Identify the blood parasite species.
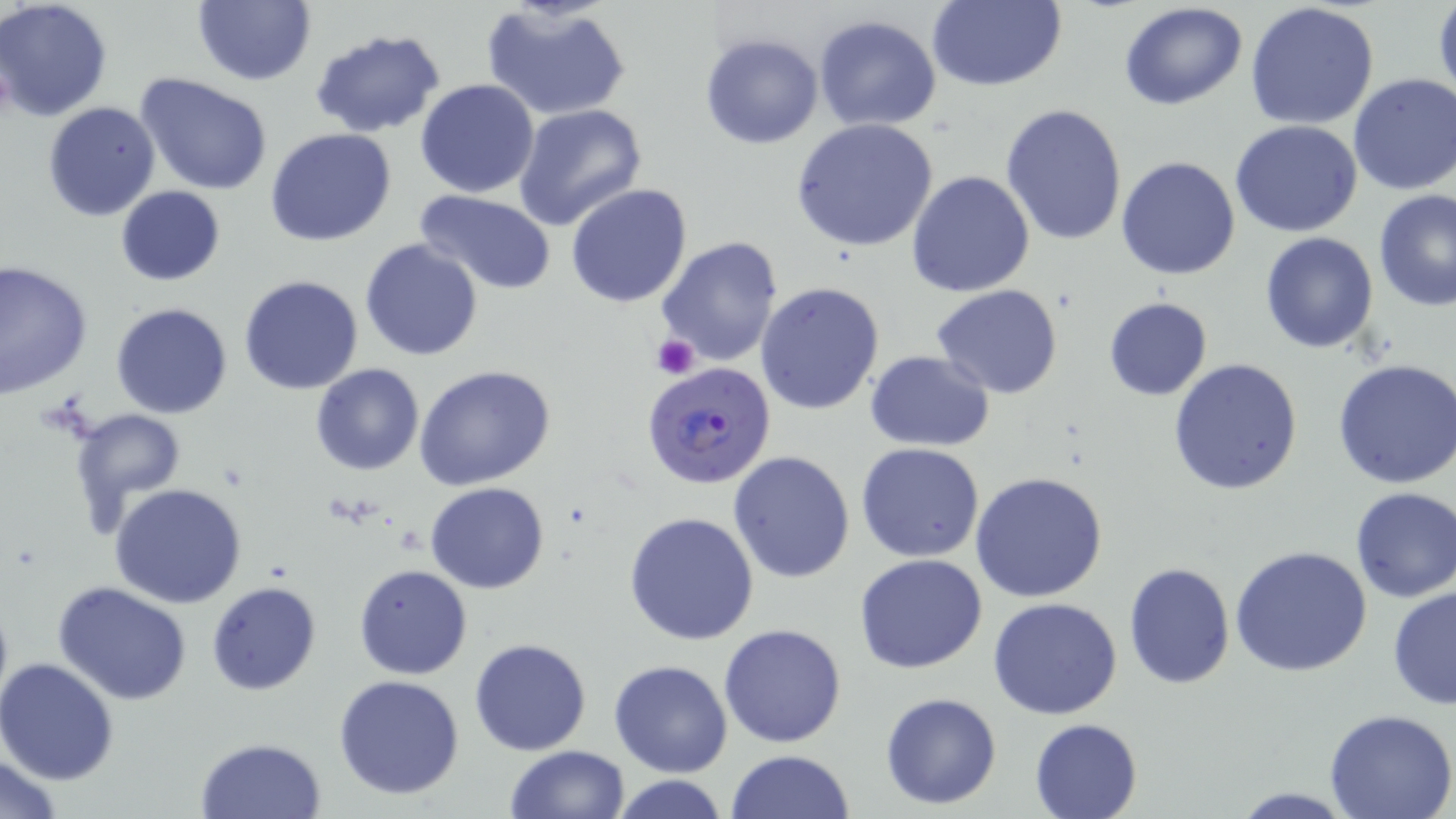

Plasmodium falciparum.

Summary:
  - Coordinate format: approximate bounding boxes as named x1/y1/x2/y2 corners in pixels
  - Platelet locations: (x1=652, y1=333, x2=700, y2=379)
  - Plasmodium falciparum-infected red blood cell locations: (x1=644, y1=361, x2=776, y2=487)
  - Uninfected red blood cell locations: (x1=0, y1=0, x2=114, y2=122), (x1=192, y1=0, x2=315, y2=86), (x1=924, y1=0, x2=1066, y2=91), (x1=480, y1=2, x2=632, y2=123), (x1=1120, y1=2, x2=1249, y2=111), (x1=1244, y1=2, x2=1380, y2=130), (x1=1432, y1=3, x2=1456, y2=104), (x1=813, y1=15, x2=943, y2=132), (x1=310, y1=29, x2=445, y2=137), (x1=699, y1=32, x2=825, y2=150), (x1=135, y1=72, x2=274, y2=196), (x1=1348, y1=72, x2=1456, y2=196), (x1=414, y1=80, x2=540, y2=199), (x1=44, y1=101, x2=160, y2=221), (x1=513, y1=104, x2=647, y2=231), (x1=1000, y1=104, x2=1128, y2=249), (x1=790, y1=117, x2=940, y2=254), (x1=1229, y1=119, x2=1362, y2=238), (x1=265, y1=128, x2=397, y2=247), (x1=1116, y1=155, x2=1240, y2=281), (x1=906, y1=169, x2=1035, y2=298), (x1=565, y1=183, x2=693, y2=307), (x1=115, y1=185, x2=225, y2=286), (x1=415, y1=191, x2=558, y2=295), (x1=1374, y1=191, x2=1456, y2=312), (x1=1260, y1=232, x2=1378, y2=353), (x1=656, y1=236, x2=785, y2=369), (x1=359, y1=239, x2=484, y2=361), (x1=0, y1=261, x2=94, y2=399), (x1=239, y1=274, x2=364, y2=394), (x1=756, y1=280, x2=886, y2=414), (x1=932, y1=285, x2=1064, y2=399), (x1=1103, y1=297, x2=1212, y2=401), (x1=111, y1=302, x2=233, y2=419), (x1=865, y1=350, x2=995, y2=452), (x1=1167, y1=357, x2=1304, y2=496), (x1=1333, y1=358, x2=1456, y2=488), (x1=311, y1=364, x2=423, y2=476), (x1=414, y1=365, x2=555, y2=491), (x1=67, y1=406, x2=186, y2=528), (x1=856, y1=443, x2=985, y2=563), (x1=729, y1=451, x2=856, y2=582), (x1=970, y1=471, x2=1109, y2=603), (x1=425, y1=482, x2=550, y2=594), (x1=109, y1=484, x2=248, y2=609), (x1=1350, y1=487, x2=1456, y2=603), (x1=625, y1=511, x2=760, y2=646), (x1=1229, y1=546, x2=1373, y2=679), (x1=854, y1=554, x2=988, y2=674), (x1=1123, y1=563, x2=1235, y2=688), (x1=354, y1=564, x2=472, y2=679), (x1=205, y1=579, x2=322, y2=696), (x1=53, y1=581, x2=192, y2=704), (x1=1386, y1=586, x2=1456, y2=710), (x1=988, y1=598, x2=1123, y2=720), (x1=719, y1=623, x2=848, y2=748), (x1=469, y1=638, x2=594, y2=756), (x1=0, y1=658, x2=120, y2=786), (x1=609, y1=659, x2=733, y2=778), (x1=333, y1=674, x2=467, y2=801), (x1=880, y1=692, x2=1002, y2=810), (x1=1325, y1=710, x2=1456, y2=819), (x1=1029, y1=718, x2=1144, y2=819), (x1=194, y1=736, x2=328, y2=818), (x1=504, y1=745, x2=630, y2=819), (x1=726, y1=749, x2=855, y2=819), (x1=2, y1=753, x2=65, y2=817), (x1=606, y1=774, x2=735, y2=819), (x1=1226, y1=788, x2=1362, y2=817)
  - Preparation: thin blood smear
  - Field of view: one of a larger specimen
  - Image size: 1456×819 pixels
  - Stain: May-Grünwald-Giemsa
  - Modality: optical microscopy
  - Magnification: 1000x